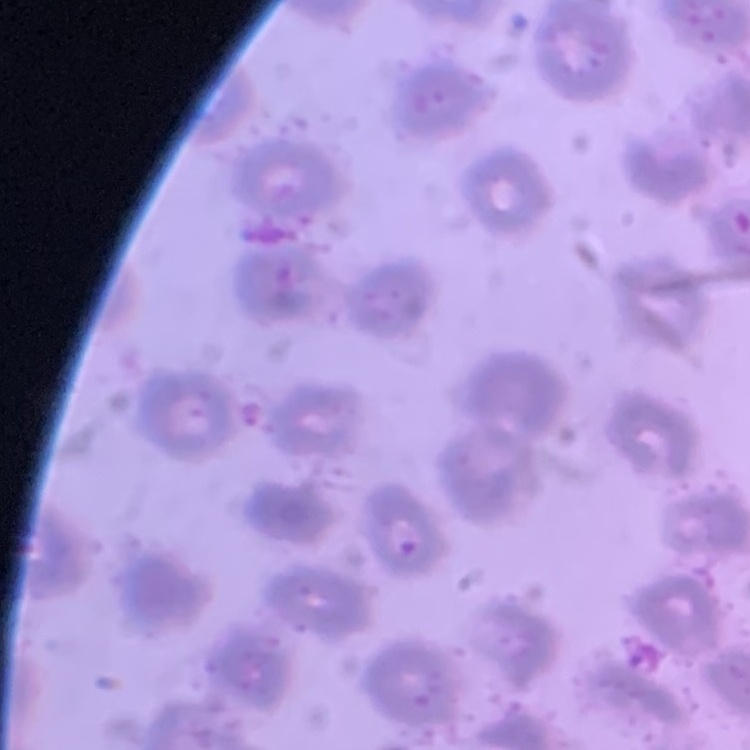

Summary:
  - Erythrocyte morphology: no rouleaux formation
  - Stain: Field's or Giemsa
  - Preparation: thin blood smear
  - Image type: one tile cut from a larger photomicrograph